Classify this cell by malaria status.
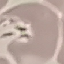
Uninfected.

Summary:
  - Preparation: thin blood film
  - Image type: automatically extracted cell patch, resized to 64 × 64 pixels
  - Stain: Giemsa
  - Capture: smartphone camera at the microscope eyepiece